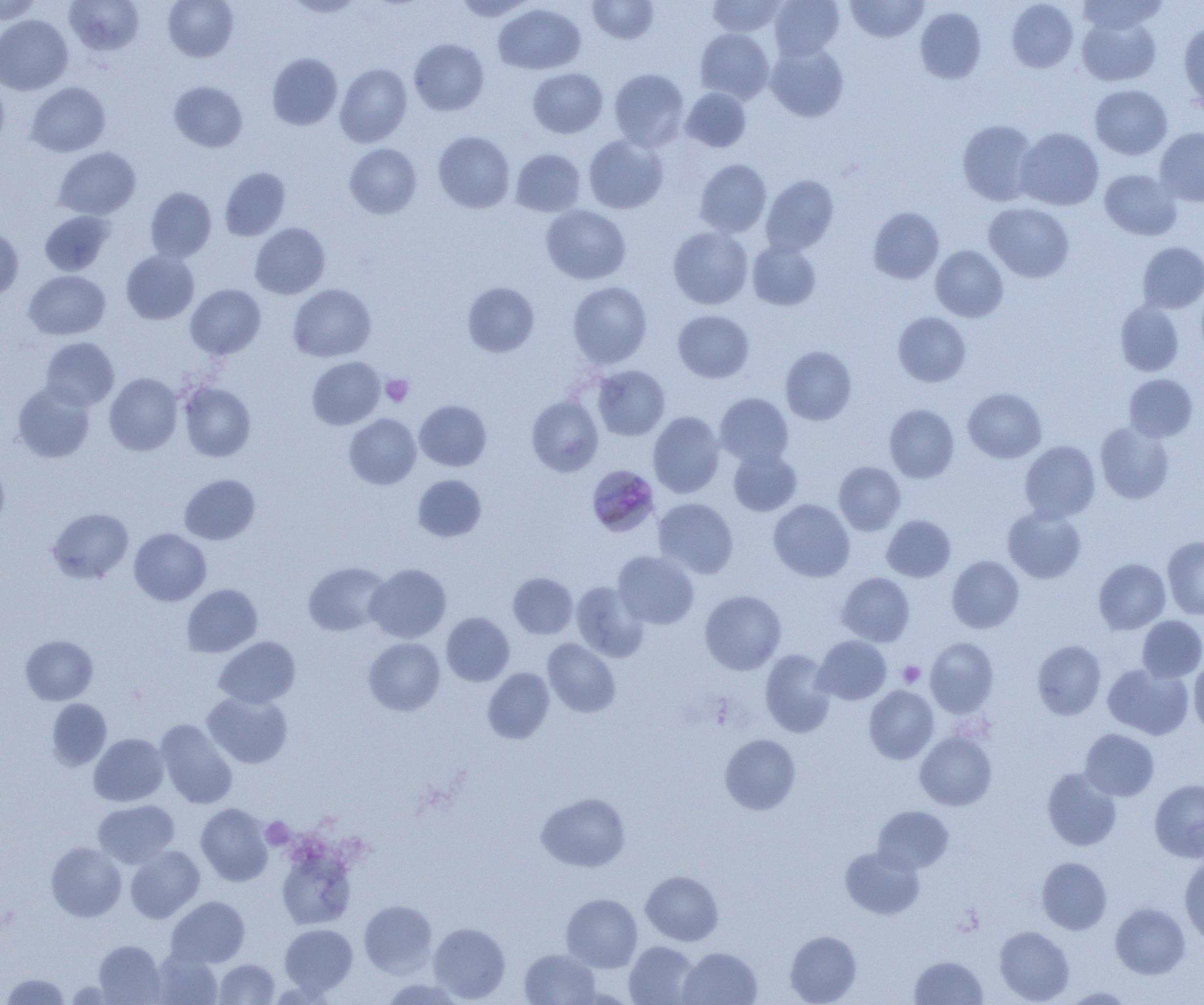
Approximate bounding boxes as named x1/y1/x2/y2 corners in pixels. Platelet locations: (x1=381, y1=375, x2=413, y2=407), (x1=898, y1=661, x2=925, y2=687), (x1=261, y1=817, x2=293, y2=849). Plasmodium malariae-infected red blood cell locations: (x1=587, y1=467, x2=658, y2=537). Uninfected red blood cell locations: (x1=0, y1=0, x2=42, y2=23), (x1=163, y1=0, x2=238, y2=61), (x1=286, y1=0, x2=364, y2=18), (x1=453, y1=0, x2=536, y2=20), (x1=587, y1=0, x2=659, y2=44), (x1=707, y1=0, x2=786, y2=36), (x1=769, y1=0, x2=844, y2=61), (x1=846, y1=0, x2=927, y2=42), (x1=1076, y1=0, x2=1167, y2=35), (x1=64, y1=1, x2=144, y2=56), (x1=1007, y1=1, x2=1078, y2=72), (x1=494, y1=3, x2=585, y2=74), (x1=915, y1=7, x2=986, y2=84), (x1=1076, y1=14, x2=1161, y2=86), (x1=0, y1=15, x2=72, y2=95), (x1=1179, y1=23, x2=1204, y2=111), (x1=695, y1=28, x2=774, y2=103), (x1=409, y1=39, x2=488, y2=115), (x1=766, y1=43, x2=848, y2=122), (x1=267, y1=53, x2=342, y2=129), (x1=335, y1=63, x2=412, y2=147), (x1=528, y1=68, x2=607, y2=138), (x1=609, y1=69, x2=689, y2=150), (x1=0, y1=80, x2=9, y2=150), (x1=169, y1=81, x2=247, y2=152), (x1=26, y1=82, x2=110, y2=157), (x1=1090, y1=85, x2=1172, y2=159), (x1=681, y1=88, x2=751, y2=152), (x1=957, y1=120, x2=1039, y2=206), (x1=1016, y1=127, x2=1103, y2=210), (x1=1155, y1=128, x2=1204, y2=206), (x1=433, y1=131, x2=514, y2=212), (x1=584, y1=134, x2=668, y2=213), (x1=344, y1=143, x2=421, y2=218), (x1=54, y1=147, x2=141, y2=219), (x1=511, y1=149, x2=585, y2=216), (x1=695, y1=159, x2=771, y2=237), (x1=220, y1=167, x2=290, y2=240), (x1=1099, y1=169, x2=1181, y2=240), (x1=761, y1=174, x2=838, y2=255), (x1=146, y1=187, x2=216, y2=262), (x1=984, y1=202, x2=1074, y2=282), (x1=541, y1=205, x2=631, y2=285), (x1=868, y1=207, x2=944, y2=284), (x1=39, y1=210, x2=114, y2=275), (x1=250, y1=223, x2=329, y2=299), (x1=668, y1=226, x2=753, y2=309), (x1=0, y1=227, x2=23, y2=300), (x1=747, y1=240, x2=821, y2=311), (x1=1137, y1=242, x2=1204, y2=313), (x1=930, y1=245, x2=1008, y2=322), (x1=121, y1=250, x2=199, y2=324), (x1=24, y1=270, x2=110, y2=339), (x1=567, y1=281, x2=652, y2=368), (x1=463, y1=282, x2=539, y2=357), (x1=186, y1=284, x2=265, y2=359), (x1=288, y1=284, x2=376, y2=362), (x1=1195, y1=289, x2=1204, y2=362), (x1=1115, y1=301, x2=1184, y2=376), (x1=673, y1=310, x2=754, y2=383), (x1=893, y1=312, x2=970, y2=386), (x1=40, y1=337, x2=118, y2=410), (x1=781, y1=346, x2=856, y2=425), (x1=307, y1=357, x2=384, y2=429), (x1=591, y1=365, x2=670, y2=441), (x1=104, y1=373, x2=183, y2=456), (x1=1123, y1=374, x2=1198, y2=442), (x1=13, y1=382, x2=95, y2=462), (x1=179, y1=382, x2=255, y2=462), (x1=963, y1=388, x2=1046, y2=462), (x1=715, y1=393, x2=794, y2=469), (x1=527, y1=395, x2=603, y2=476), (x1=414, y1=400, x2=491, y2=471), (x1=884, y1=404, x2=959, y2=482), (x1=648, y1=412, x2=724, y2=498), (x1=344, y1=414, x2=421, y2=489), (x1=1095, y1=421, x2=1174, y2=504), (x1=1019, y1=441, x2=1100, y2=522), (x1=728, y1=448, x2=802, y2=516), (x1=0, y1=457, x2=9, y2=535), (x1=834, y1=462, x2=905, y2=535), (x1=179, y1=474, x2=260, y2=544), (x1=413, y1=474, x2=486, y2=542), (x1=654, y1=498, x2=738, y2=578), (x1=769, y1=499, x2=854, y2=582), (x1=48, y1=507, x2=133, y2=583), (x1=1003, y1=507, x2=1086, y2=583), (x1=882, y1=515, x2=955, y2=581), (x1=129, y1=528, x2=211, y2=606), (x1=1162, y1=536, x2=1204, y2=620), (x1=613, y1=551, x2=698, y2=629), (x1=947, y1=556, x2=1023, y2=633), (x1=1094, y1=559, x2=1170, y2=634), (x1=303, y1=562, x2=391, y2=636), (x1=365, y1=563, x2=451, y2=643), (x1=508, y1=572, x2=577, y2=639), (x1=837, y1=573, x2=914, y2=646), (x1=572, y1=581, x2=649, y2=661), (x1=182, y1=584, x2=262, y2=657), (x1=700, y1=590, x2=786, y2=674), (x1=441, y1=612, x2=514, y2=686), (x1=1137, y1=616, x2=1204, y2=683), (x1=21, y1=635, x2=97, y2=705), (x1=214, y1=636, x2=300, y2=708), (x1=813, y1=636, x2=891, y2=705), (x1=363, y1=637, x2=445, y2=715), (x1=925, y1=637, x2=998, y2=717), (x1=543, y1=639, x2=620, y2=717), (x1=1033, y1=640, x2=1106, y2=719), (x1=760, y1=649, x2=836, y2=737), (x1=1190, y1=658, x2=1204, y2=736), (x1=1103, y1=663, x2=1193, y2=739), (x1=483, y1=668, x2=554, y2=743), (x1=865, y1=686, x2=939, y2=763), (x1=203, y1=691, x2=292, y2=769), (x1=46, y1=699, x2=111, y2=769), (x1=156, y1=719, x2=237, y2=809), (x1=1080, y1=729, x2=1158, y2=801), (x1=915, y1=732, x2=996, y2=810), (x1=89, y1=733, x2=169, y2=806), (x1=720, y1=734, x2=800, y2=814), (x1=1043, y1=767, x2=1121, y2=851), (x1=1150, y1=779, x2=1204, y2=862), (x1=536, y1=792, x2=630, y2=872), (x1=93, y1=800, x2=179, y2=868), (x1=196, y1=803, x2=274, y2=886), (x1=873, y1=806, x2=953, y2=874), (x1=46, y1=842, x2=126, y2=921), (x1=126, y1=846, x2=204, y2=923), (x1=840, y1=846, x2=924, y2=920), (x1=277, y1=848, x2=356, y2=930), (x1=1037, y1=857, x2=1111, y2=934), (x1=1180, y1=857, x2=1204, y2=944), (x1=641, y1=871, x2=723, y2=945), (x1=561, y1=893, x2=642, y2=972), (x1=166, y1=896, x2=250, y2=967), (x1=359, y1=900, x2=437, y2=977), (x1=1110, y1=903, x2=1189, y2=978), (x1=428, y1=922, x2=510, y2=1002), (x1=280, y1=924, x2=358, y2=995), (x1=994, y1=926, x2=1073, y2=1004), (x1=785, y1=930, x2=861, y2=1004), (x1=93, y1=940, x2=166, y2=1004), (x1=624, y1=941, x2=699, y2=1005), (x1=678, y1=947, x2=762, y2=1004), (x1=520, y1=949, x2=600, y2=1005), (x1=151, y1=950, x2=223, y2=1004), (x1=910, y1=956, x2=987, y2=1004), (x1=214, y1=959, x2=279, y2=1004), (x1=1, y1=972, x2=71, y2=1004), (x1=381, y1=978, x2=466, y2=1005), (x1=1064, y1=987, x2=1134, y2=1004). Slide-level diagnosis: Plasmodium malariae. One field of a larger specimen. Image is 1204×1005 pixels. Thin blood film. Optical microscopy. 1000x magnification.